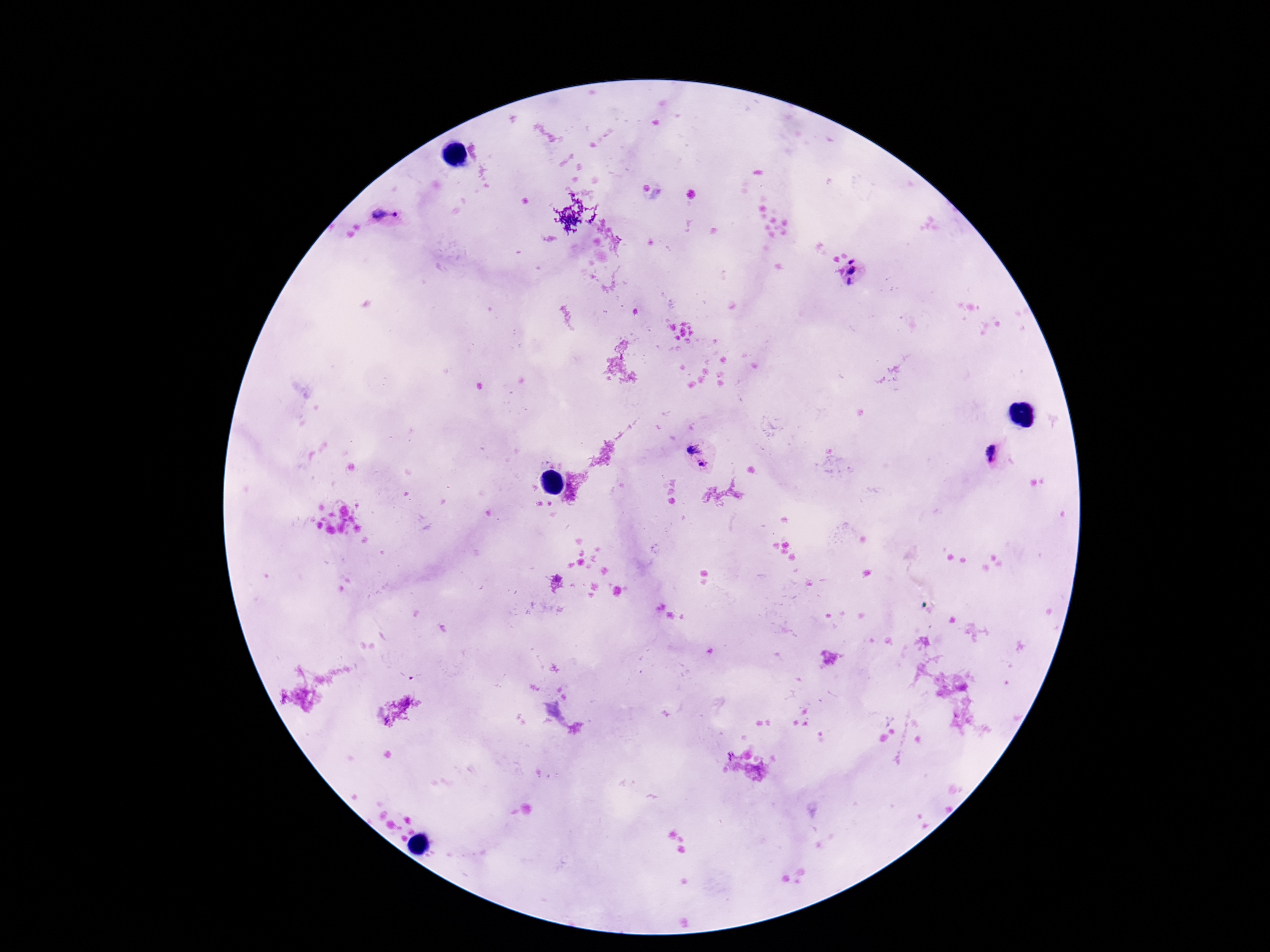

Approximate centers as {x, y} in pixels. Plasmodium parasite locations: {386, 218}, {854, 275}, {991, 455}, {700, 456}. Photographed through the microscope eyepiece with a smartphone camera. Giemsa-stained preparation. 100x magnification. Thick blood smear. Image is 1270×952 pixels. Single field of view. Patient malaria status: infected.